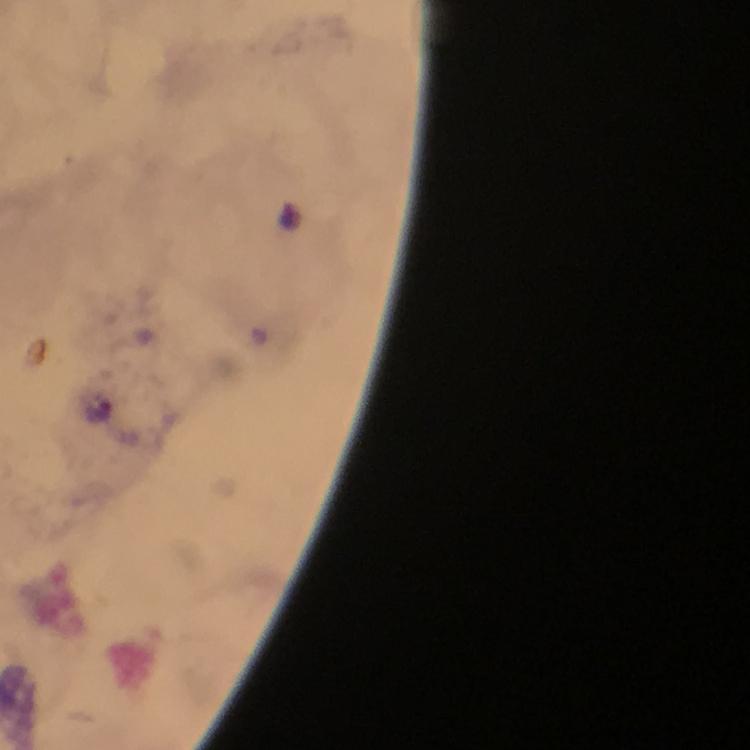
Approximate centers as {x, y} in pixels. Malaria parasite locations: {96, 414}. Image is 750×750 pixels. Immersion oil applied. Photographed through the microscope with a smartphone camera. 100x magnification. From a malaria diagnostic workup. Giemsa-stained preparation. Thick blood film. A crop from one field of view.